Give the extent of all Plasmodium falciparum-infected red blood cells.
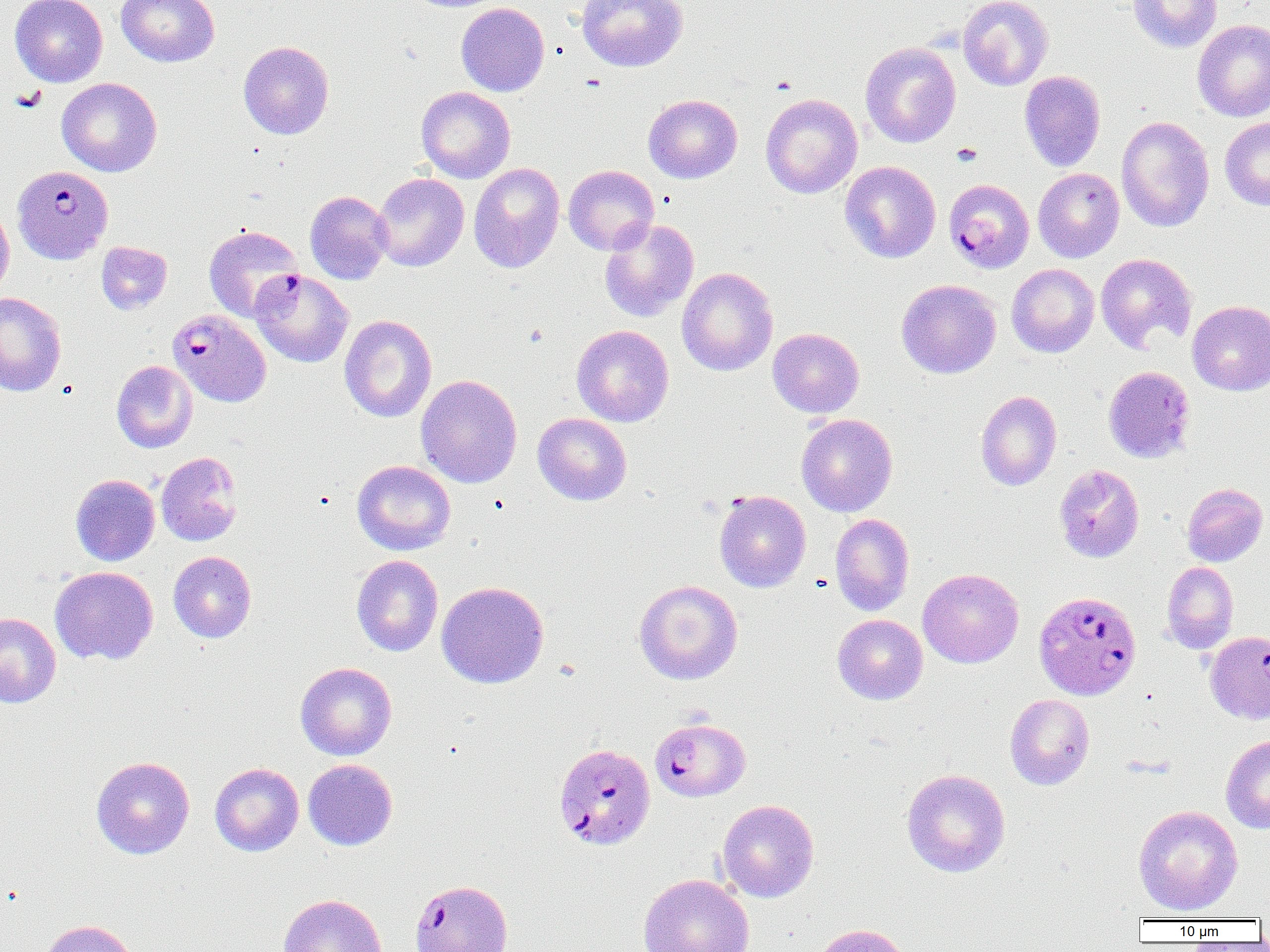

Approximate bounding boxes as [x1, y1, x2, y2] in pixels.
Plasmodium falciparum-infected red blood cells: [12, 165, 114, 264], [944, 179, 1035, 273], [250, 269, 353, 367], [168, 308, 271, 407], [1033, 590, 1142, 700], [1204, 630, 1270, 725], [650, 717, 751, 802], [553, 742, 657, 851].

Uninfected red blood cell locations: [11, 0, 108, 87], [117, 0, 219, 67], [577, 0, 688, 72], [957, 0, 1053, 91], [1128, 0, 1221, 52], [456, 2, 550, 96], [1192, 19, 1270, 122], [238, 40, 334, 139], [860, 42, 961, 148], [1019, 70, 1106, 172], [57, 77, 162, 177], [416, 86, 515, 183], [760, 93, 862, 198], [644, 94, 743, 183], [1116, 115, 1214, 232], [1220, 117, 1270, 211], [840, 161, 941, 263], [468, 162, 565, 273], [563, 165, 659, 255], [1033, 168, 1124, 262], [372, 173, 469, 271], [305, 190, 393, 284], [0, 202, 14, 299], [599, 218, 699, 323], [203, 225, 304, 322], [96, 242, 172, 314], [1095, 253, 1197, 354], [1006, 264, 1099, 358], [676, 267, 778, 376], [896, 279, 1001, 379], [0, 291, 66, 396], [1187, 301, 1270, 396], [339, 315, 437, 422], [572, 325, 674, 426], [768, 327, 865, 418], [111, 360, 197, 453], [1103, 365, 1196, 463], [416, 374, 522, 488], [975, 390, 1062, 491], [533, 413, 632, 505], [796, 414, 897, 517], [156, 451, 243, 546], [352, 460, 456, 555], [1054, 464, 1144, 563], [70, 474, 160, 566], [1181, 483, 1268, 566], [714, 489, 811, 593], [830, 513, 915, 616], [168, 551, 256, 643], [352, 554, 444, 657], [1161, 561, 1238, 654], [50, 566, 158, 665], [917, 568, 1024, 668], [634, 579, 743, 685], [436, 581, 549, 689], [0, 612, 61, 708], [832, 614, 928, 705], [295, 662, 397, 760], [1005, 693, 1095, 790], [1220, 736, 1270, 834], [91, 756, 195, 859], [303, 759, 398, 851], [209, 763, 304, 856], [901, 768, 1011, 878], [717, 799, 819, 902], [1133, 805, 1243, 915], [638, 873, 754, 952], [409, 879, 513, 952], [278, 893, 388, 952], [36, 919, 140, 952], [811, 923, 911, 952]. Platelet locations: [11, 87, 47, 112], [952, 142, 982, 165]. Slide-level diagnosis: Plasmodium falciparum. Image is 1270×952 pixels. Thin blood smear. Single field of view. Captured at 1000x magnification. Light microscopy.